Comment on the morphology of the red blood cells.
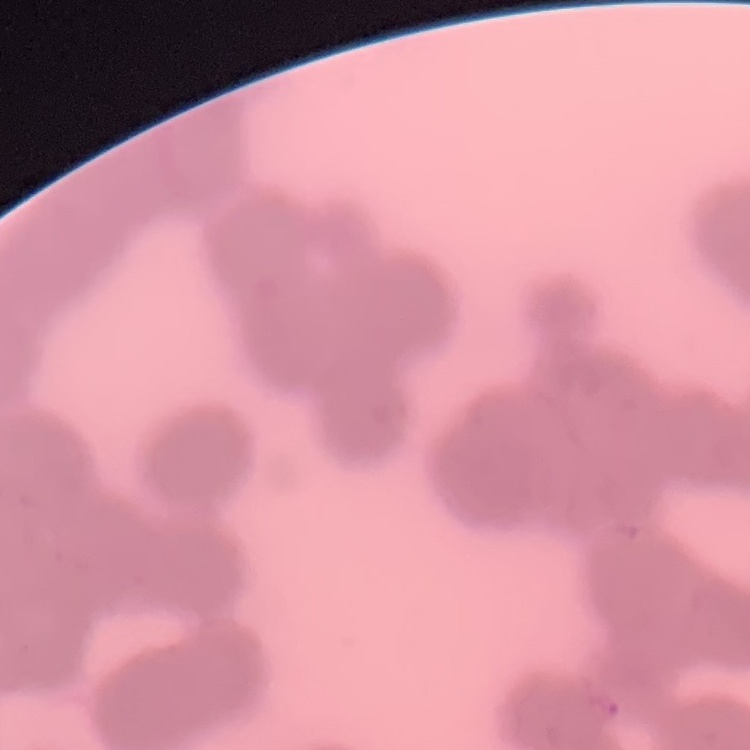

They show rouleaux formation.

One tile cut from a larger photomicrograph. Field's or Giemsa stain. Thin blood smear.